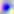
modality = micrograph
magnification = 400x
identification = Toxoplasma gondii